Outline each Plasmodium falciparum-infected red blood cell.
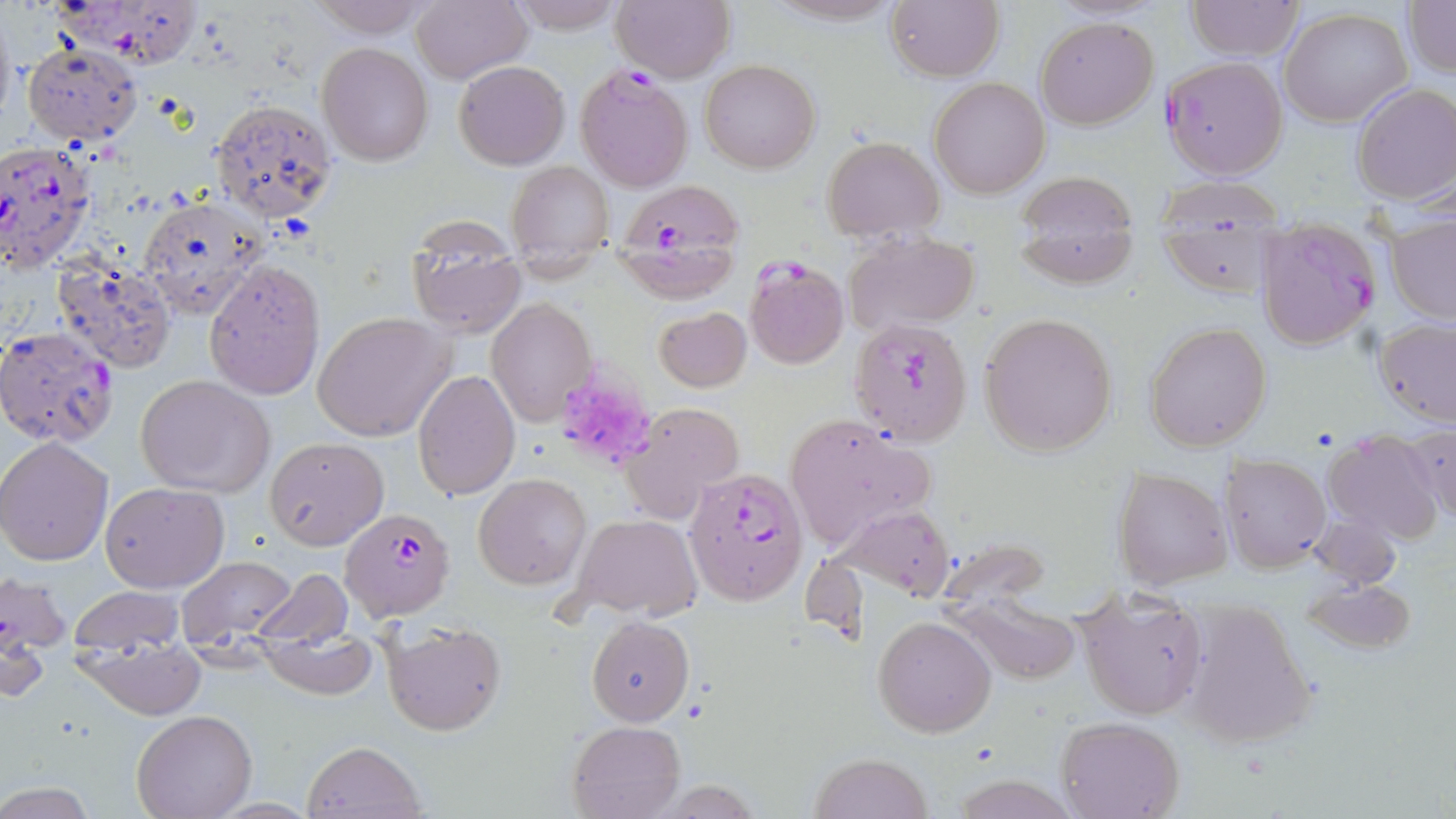

Approximate bounding boxes as (x1,y1)-(x2,y2) corner pairs in pixels.
Plasmodium falciparum-infected red blood cells: (50,0)-(155,62), (1162,56)-(1288,180), (573,63)-(693,191), (0,143)-(98,272), (614,183)-(743,300), (1255,216)-(1380,350), (744,257)-(849,369), (850,316)-(973,446), (0,326)-(119,447), (684,464)-(808,606), (341,505)-(457,623).

Platelet locations: (560,381)-(654,459). Uninfected red blood cell locations: (307,0)-(432,38), (409,0)-(529,85), (506,0)-(627,35), (762,0)-(905,27), (884,0)-(1003,81), (1404,0)-(1456,78), (612,1)-(735,83), (1186,1)-(1304,61), (1279,8)-(1411,127), (1035,16)-(1159,130), (316,42)-(433,165), (20,45)-(142,147), (700,59)-(820,173), (454,60)-(571,168), (929,77)-(1051,197), (1351,82)-(1456,206), (209,96)-(338,221), (822,137)-(944,240), (508,160)-(613,257), (1017,171)-(1138,235), (1152,176)-(1290,233), (138,195)-(267,318), (1385,213)-(1456,324), (1159,223)-(1279,298), (406,229)-(526,339), (844,232)-(982,337), (1020,233)-(1135,288), (51,253)-(177,372), (203,259)-(326,400), (485,298)-(596,425), (653,306)-(752,393), (312,311)-(456,442), (978,312)-(1119,455), (1373,319)-(1456,428), (1144,322)-(1272,451), (412,368)-(521,501), (136,374)-(276,497), (621,401)-(746,527), (785,417)-(937,546), (1400,424)-(1456,525), (1322,433)-(1443,544), (0,436)-(115,566), (263,436)-(389,549), (1220,454)-(1331,574), (1114,467)-(1231,590), (474,475)-(591,589), (101,482)-(229,593), (832,506)-(960,605), (1310,512)-(1402,590), (570,513)-(702,622), (174,554)-(302,649), (0,568)-(70,681), (250,568)-(351,650), (1301,577)-(1418,656), (66,586)-(186,656), (948,595)-(1083,686), (1177,600)-(1317,748), (1075,601)-(1212,722), (587,615)-(694,726), (872,615)-(998,738), (380,617)-(508,736), (74,628)-(205,719), (132,711)-(254,819), (1055,716)-(1185,818), (566,719)-(686,818), (301,739)-(427,818), (808,751)-(932,819), (947,770)-(1078,819). Slide-level diagnosis: Plasmodium falciparum. Captured at 1000x magnification. Image is 1456×819 pixels. Single field of view. May-Grünwald-Giemsa stain. Thin blood smear. Light microscopy.